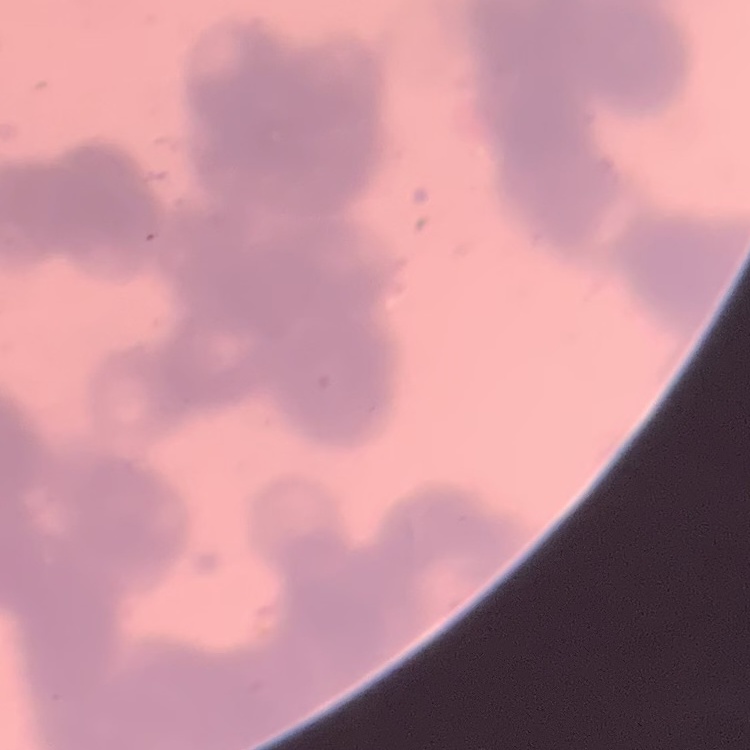

Summary:
  - Red blood cell morphology: rouleaux formation
  - Stain: Field's or Giemsa
  - Image type: one tile cut from a larger photomicrograph
  - Preparation: thin blood smear